Comment on the morphology of the erythrocytes.
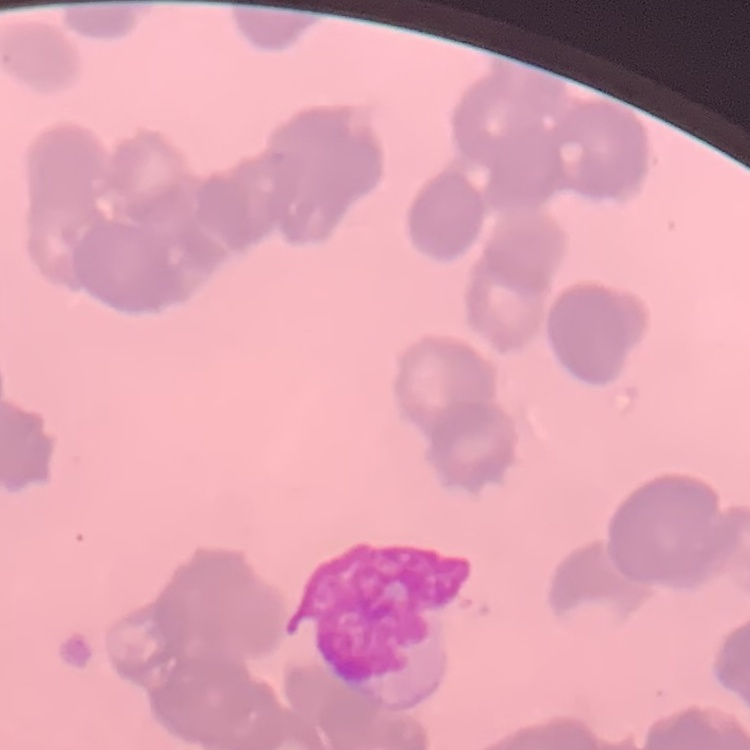

Rouleaux formation.

Summary:
  - Image type: one tile cut from a larger photomicrograph
  - Stain: Field's or Giemsa
  - Preparation: thin peripheral smear